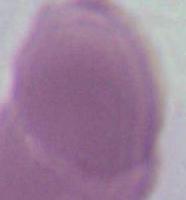
Summary:
  - Identification: red blood cell
  - Magnification: 1000x
  - Modality: photomicrograph